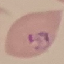 Malaria status: parasitized. Cell patch, automatically extracted from a larger field of view and resized to 64 × 64 pixels. Acquired by smartphone through the microscope eyepiece. Thin blood smear. Giemsa-stained preparation.